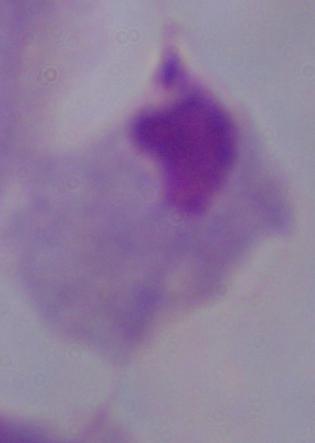
magnification: 1000x
identification: trichomonad
modality: photomicrograph